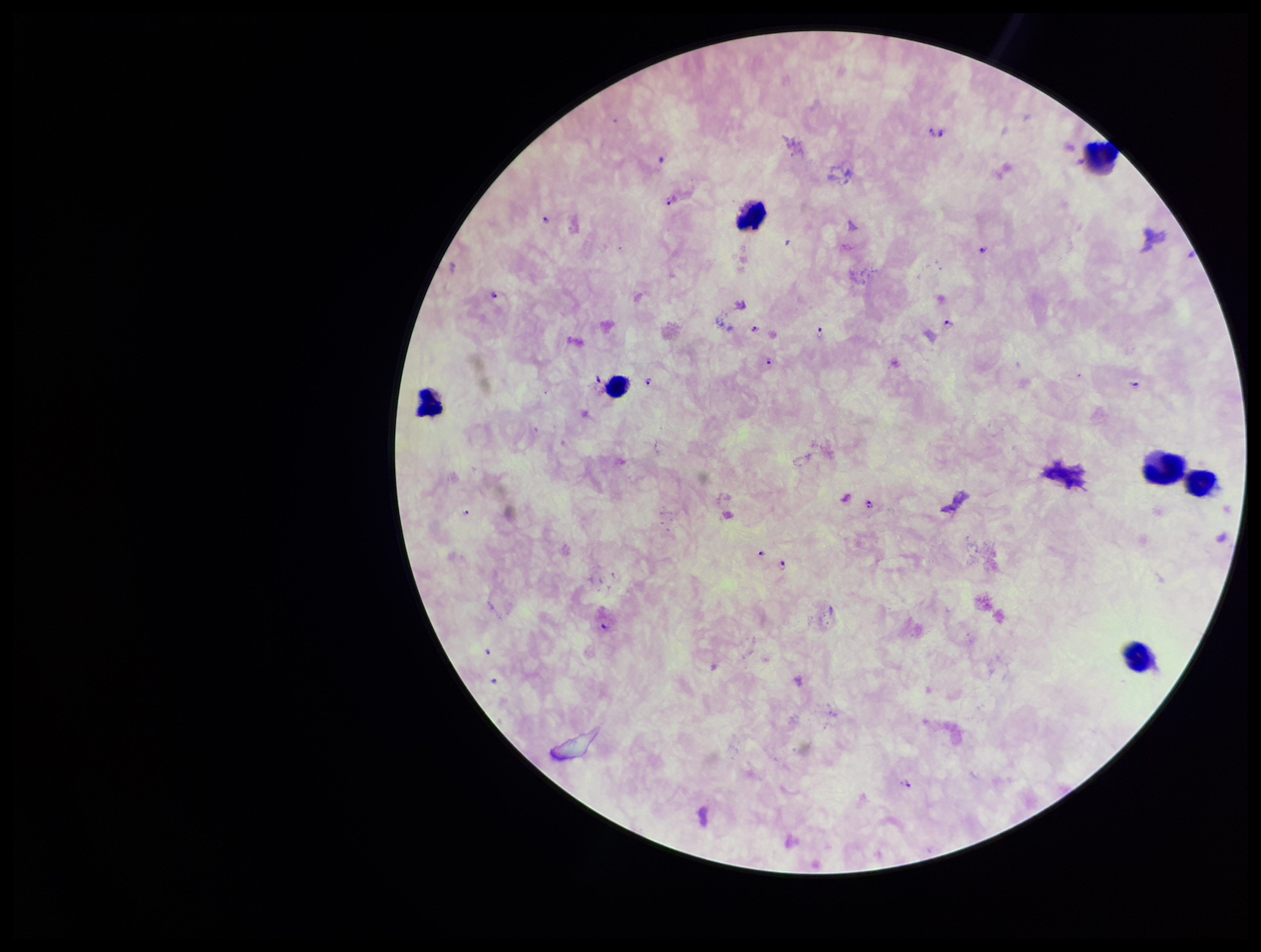

plasmodium_parasites: seen
image_size: 1261×952 pixels
parasite_count: 18
capture: smartphone photograph through the microscope eyepiece
field_of_view: single
species_reported_for_this_patient: Plasmodium falciparum
patient_malaria_status: positive
leukocyte_count: 7
stain: Giemsa
preparation: thick smear